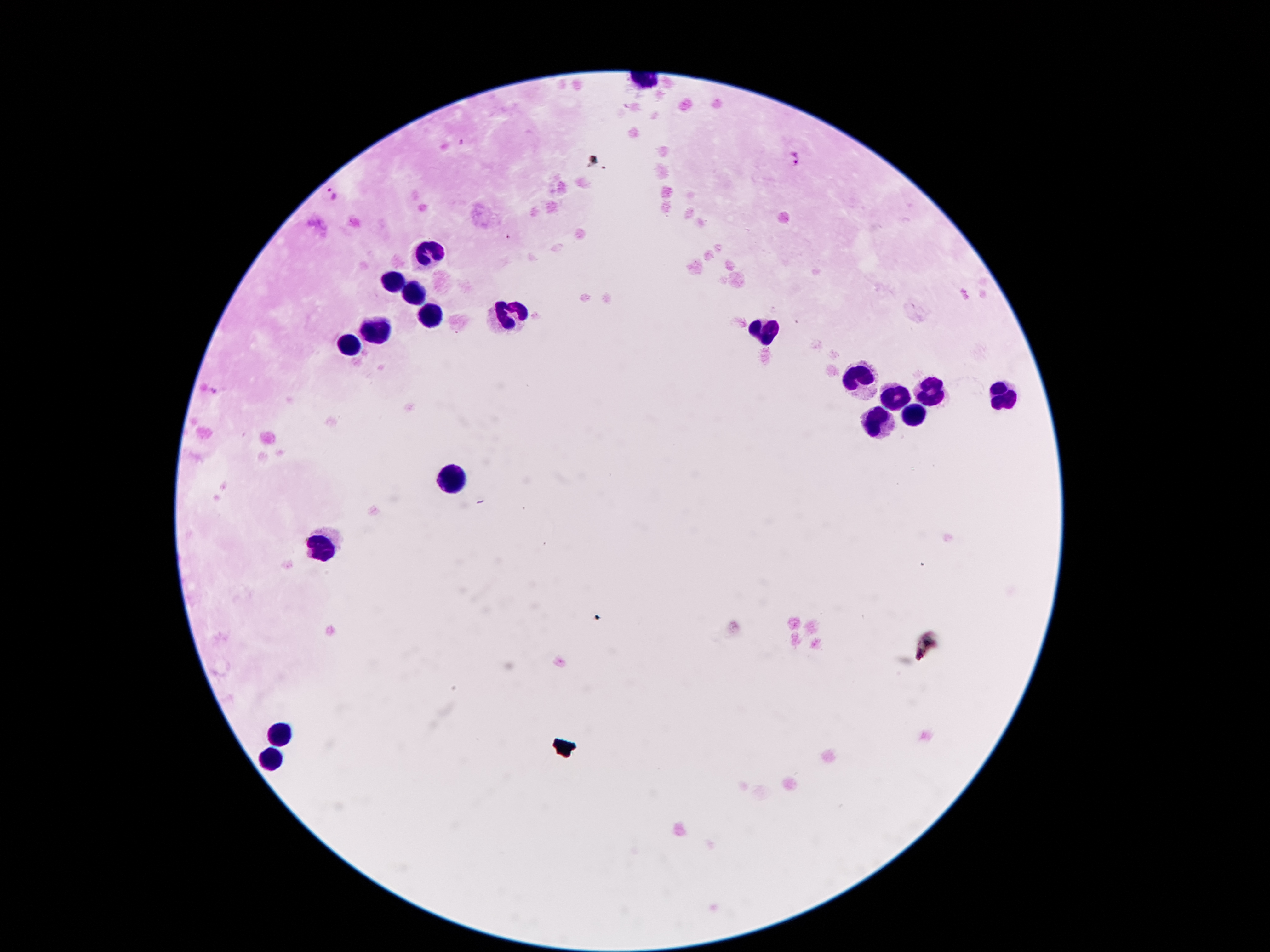 Approximate centers as [x, y] in pixels. Plasmodium parasite locations: [797, 157], [332, 191]. Leukocyte locations: [426, 254], [392, 281], [412, 294], [428, 314], [507, 314], [764, 329], [373, 332], [351, 345], [861, 378], [930, 393], [896, 396], [1002, 400], [910, 416], [879, 422], [450, 478], [320, 550], [282, 734], [271, 760]. Giemsa-stained preparation. Thick peripheral-blood smear. Single field of view. Patient malaria status: positive for Plasmodium falciparum. 100x magnification. Image is 1270×952 pixels. Smartphone photograph taken through the microscope eyepiece.